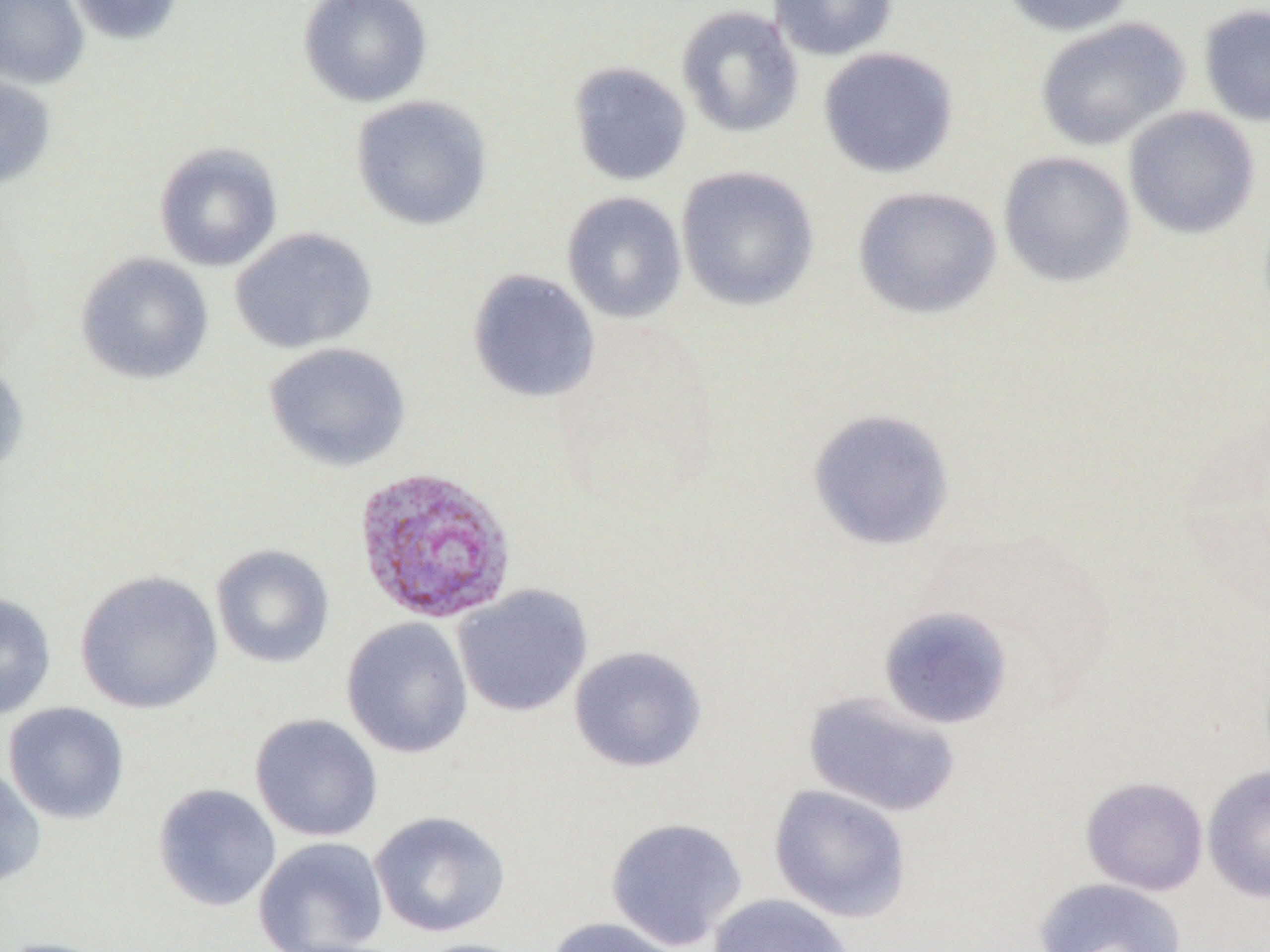 Approximate bounding boxes as (x1,y1)-(x2,y2) corner pairs in pixels. Uninfected red blood cell locations: (0,0)-(89,89), (65,0)-(185,45), (298,0)-(434,108), (768,0)-(898,61), (997,0)-(1137,37), (1198,3)-(1270,128), (676,6)-(804,138), (1034,17)-(1190,151), (818,47)-(959,178), (567,62)-(693,186), (0,70)-(57,192), (350,95)-(493,231), (1123,106)-(1260,239), (153,142)-(283,272), (997,150)-(1136,288), (676,166)-(820,312), (852,186)-(1001,319), (561,191)-(687,324), (230,227)-(377,354), (75,252)-(214,385), (467,268)-(601,404), (265,341)-(410,472), (0,360)-(30,477), (807,408)-(956,551), (210,543)-(336,668), (74,569)-(223,714), (452,584)-(593,718), (0,591)-(56,721), (878,605)-(1015,729), (341,617)-(474,759), (569,645)-(707,773), (803,689)-(961,818), (3,702)-(130,825), (249,713)-(383,842), (0,763)-(47,890), (1202,764)-(1270,903), (1080,775)-(1209,896), (152,783)-(282,912), (767,784)-(912,923), (370,811)-(512,938), (605,816)-(748,950), (253,837)-(389,951), (1034,877)-(1187,952), (706,893)-(855,952), (542,916)-(687,952), (0,937)-(118,952), (406,938)-(535,952). Plasmodium vivax-infected red blood cell locations: (352,466)-(519,625). Slide-level diagnosis: Plasmodium vivax. Thin blood smear. One field of a larger specimen. Image is 1270×952 pixels. Light microscopy. 1000x magnification.